Locate every Plasmodium falciparum-infected red blood cell.
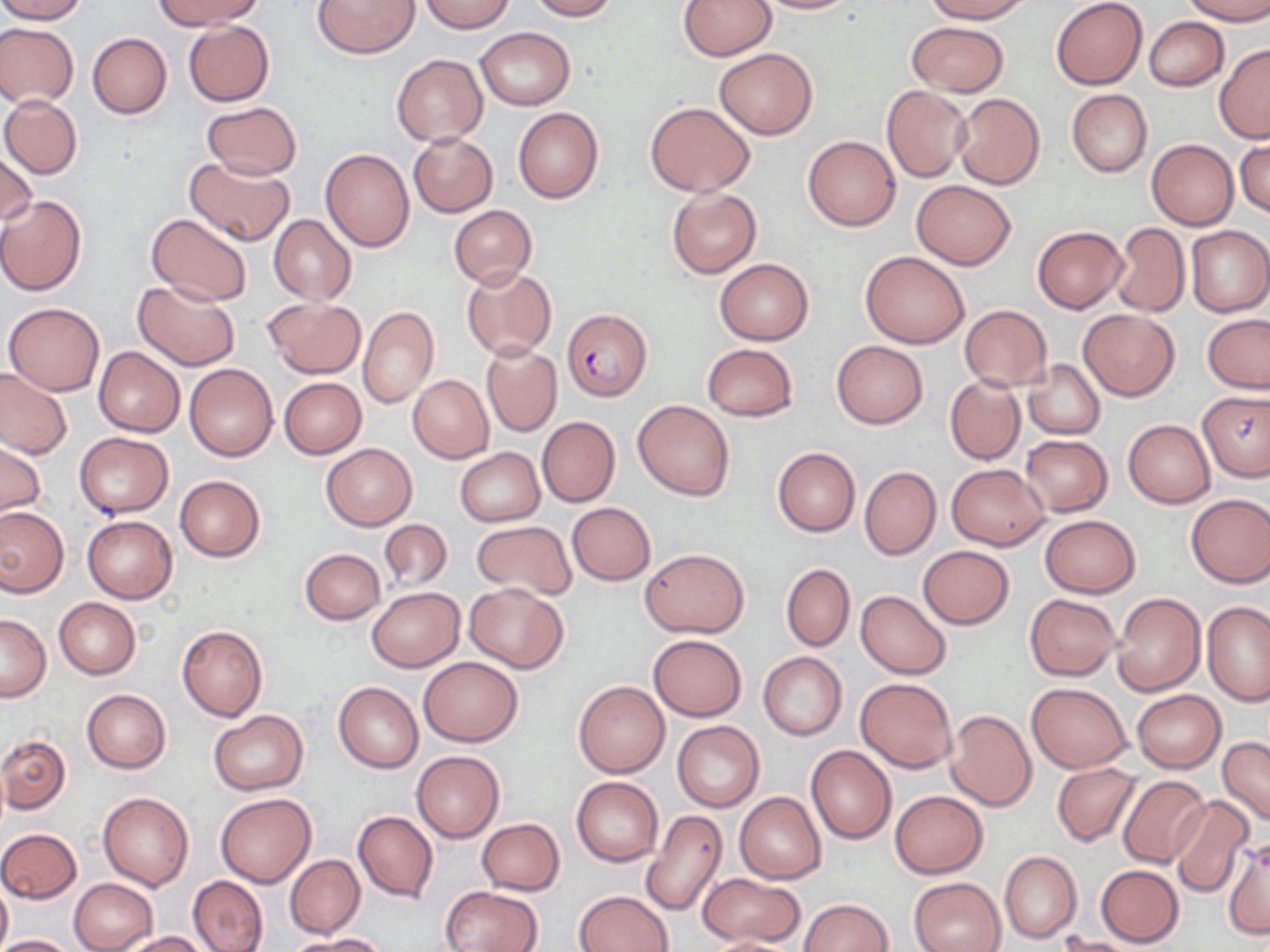

Approximate bounding boxes as named x1/y1/x2/y2 corners in pixels.
Plasmodium falciparum-infected red blood cells: (x1=562, y1=308, x2=651, y2=401).

Summary:
  - Uninfected red blood cell locations: (x1=0, y1=0, x2=88, y2=23), (x1=156, y1=0, x2=261, y2=29), (x1=314, y1=0, x2=419, y2=58), (x1=419, y1=0, x2=515, y2=32), (x1=527, y1=0, x2=618, y2=21), (x1=678, y1=0, x2=775, y2=61), (x1=750, y1=0, x2=860, y2=14), (x1=923, y1=0, x2=1032, y2=23), (x1=1181, y1=0, x2=1270, y2=23), (x1=1051, y1=1, x2=1147, y2=89), (x1=1144, y1=17, x2=1228, y2=91), (x1=181, y1=20, x2=275, y2=105), (x1=906, y1=21, x2=1010, y2=96), (x1=0, y1=23, x2=78, y2=107), (x1=476, y1=27, x2=575, y2=110), (x1=88, y1=33, x2=171, y2=119), (x1=1214, y1=44, x2=1270, y2=143), (x1=714, y1=47, x2=818, y2=138), (x1=391, y1=53, x2=488, y2=147), (x1=881, y1=85, x2=972, y2=182), (x1=1066, y1=88, x2=1152, y2=177), (x1=952, y1=93, x2=1045, y2=189), (x1=1, y1=94, x2=83, y2=180), (x1=645, y1=101, x2=755, y2=196), (x1=201, y1=102, x2=301, y2=179), (x1=513, y1=107, x2=604, y2=203), (x1=408, y1=132, x2=497, y2=217), (x1=802, y1=135, x2=901, y2=231), (x1=1147, y1=139, x2=1238, y2=230), (x1=1234, y1=139, x2=1270, y2=219), (x1=320, y1=148, x2=415, y2=251), (x1=0, y1=149, x2=36, y2=230), (x1=185, y1=155, x2=295, y2=247), (x1=911, y1=180, x2=1017, y2=269), (x1=667, y1=188, x2=762, y2=279), (x1=0, y1=196, x2=86, y2=296), (x1=449, y1=205, x2=536, y2=290), (x1=146, y1=212, x2=253, y2=306), (x1=268, y1=214, x2=357, y2=305), (x1=1110, y1=224, x2=1190, y2=317), (x1=1185, y1=225, x2=1269, y2=317), (x1=1033, y1=226, x2=1127, y2=312), (x1=861, y1=250, x2=970, y2=348), (x1=714, y1=258, x2=813, y2=345), (x1=462, y1=267, x2=556, y2=360), (x1=132, y1=280, x2=240, y2=371), (x1=263, y1=297, x2=366, y2=379), (x1=4, y1=302, x2=105, y2=396), (x1=358, y1=305, x2=440, y2=409), (x1=958, y1=305, x2=1051, y2=390), (x1=1079, y1=309, x2=1179, y2=400), (x1=1202, y1=313, x2=1270, y2=393), (x1=831, y1=341, x2=928, y2=428), (x1=701, y1=342, x2=798, y2=420), (x1=480, y1=344, x2=561, y2=437), (x1=93, y1=346, x2=185, y2=437), (x1=1023, y1=359, x2=1104, y2=439), (x1=184, y1=363, x2=278, y2=461), (x1=0, y1=367, x2=72, y2=460), (x1=407, y1=374, x2=493, y2=463), (x1=278, y1=376, x2=365, y2=459), (x1=945, y1=376, x2=1025, y2=465), (x1=1199, y1=390, x2=1270, y2=482), (x1=633, y1=400, x2=735, y2=499), (x1=537, y1=417, x2=620, y2=507), (x1=1124, y1=420, x2=1216, y2=507), (x1=73, y1=431, x2=174, y2=517), (x1=1021, y1=435, x2=1112, y2=516), (x1=0, y1=441, x2=45, y2=519), (x1=322, y1=443, x2=416, y2=531), (x1=772, y1=446, x2=860, y2=536), (x1=454, y1=447, x2=544, y2=526), (x1=946, y1=464, x2=1050, y2=549), (x1=859, y1=465, x2=941, y2=559), (x1=174, y1=476, x2=265, y2=563), (x1=1185, y1=494, x2=1270, y2=587), (x1=566, y1=502, x2=656, y2=585), (x1=0, y1=506, x2=67, y2=596), (x1=1039, y1=515, x2=1141, y2=598), (x1=82, y1=516, x2=177, y2=603), (x1=378, y1=519, x2=451, y2=592), (x1=472, y1=520, x2=575, y2=601), (x1=918, y1=545, x2=1014, y2=629), (x1=640, y1=547, x2=748, y2=637), (x1=299, y1=548, x2=385, y2=625), (x1=781, y1=563, x2=855, y2=651), (x1=465, y1=583, x2=569, y2=672), (x1=367, y1=587, x2=464, y2=672), (x1=855, y1=590, x2=951, y2=679), (x1=1112, y1=592, x2=1205, y2=696), (x1=1024, y1=593, x2=1122, y2=681), (x1=55, y1=598, x2=139, y2=679), (x1=1202, y1=601, x2=1270, y2=706), (x1=0, y1=613, x2=51, y2=702), (x1=177, y1=624, x2=268, y2=722), (x1=647, y1=634, x2=747, y2=721), (x1=757, y1=652, x2=847, y2=740), (x1=418, y1=656, x2=524, y2=746), (x1=855, y1=677, x2=959, y2=773), (x1=573, y1=680, x2=670, y2=777), (x1=333, y1=681, x2=423, y2=772), (x1=1026, y1=682, x2=1131, y2=772), (x1=82, y1=688, x2=171, y2=773), (x1=1131, y1=689, x2=1225, y2=773), (x1=944, y1=709, x2=1037, y2=810), (x1=208, y1=710, x2=308, y2=795), (x1=672, y1=720, x2=764, y2=812), (x1=0, y1=733, x2=70, y2=815), (x1=1217, y1=736, x2=1270, y2=828), (x1=806, y1=745, x2=897, y2=846), (x1=412, y1=750, x2=504, y2=842), (x1=1051, y1=762, x2=1141, y2=847), (x1=1117, y1=775, x2=1211, y2=869), (x1=572, y1=776, x2=664, y2=867), (x1=890, y1=790, x2=989, y2=878), (x1=98, y1=791, x2=194, y2=891), (x1=736, y1=791, x2=826, y2=884), (x1=215, y1=793, x2=316, y2=887), (x1=1168, y1=795, x2=1255, y2=898), (x1=640, y1=809, x2=728, y2=917), (x1=352, y1=810, x2=439, y2=903), (x1=477, y1=818, x2=565, y2=895), (x1=0, y1=827, x2=82, y2=903), (x1=1222, y1=837, x2=1269, y2=941), (x1=999, y1=850, x2=1082, y2=944), (x1=285, y1=854, x2=364, y2=938), (x1=1096, y1=865, x2=1183, y2=946), (x1=698, y1=872, x2=805, y2=945), (x1=187, y1=875, x2=268, y2=952), (x1=910, y1=876, x2=1005, y2=952), (x1=70, y1=877, x2=158, y2=952), (x1=0, y1=880, x2=12, y2=952), (x1=442, y1=886, x2=542, y2=952), (x1=575, y1=890, x2=674, y2=952), (x1=800, y1=898, x2=893, y2=951), (x1=120, y1=931, x2=209, y2=951), (x1=0, y1=934, x2=78, y2=952), (x1=296, y1=934, x2=388, y2=951), (x1=1056, y1=934, x2=1142, y2=952), (x1=703, y1=937, x2=802, y2=951)
  - Slide-level diagnosis: Plasmodium falciparum
  - Preparation: thin blood film
  - Image size: 1270×952 pixels
  - Stain: May-Grünwald-Giemsa
  - Magnification: 1000x
  - Modality: optical microscopy
  - Field of view: one of a larger specimen